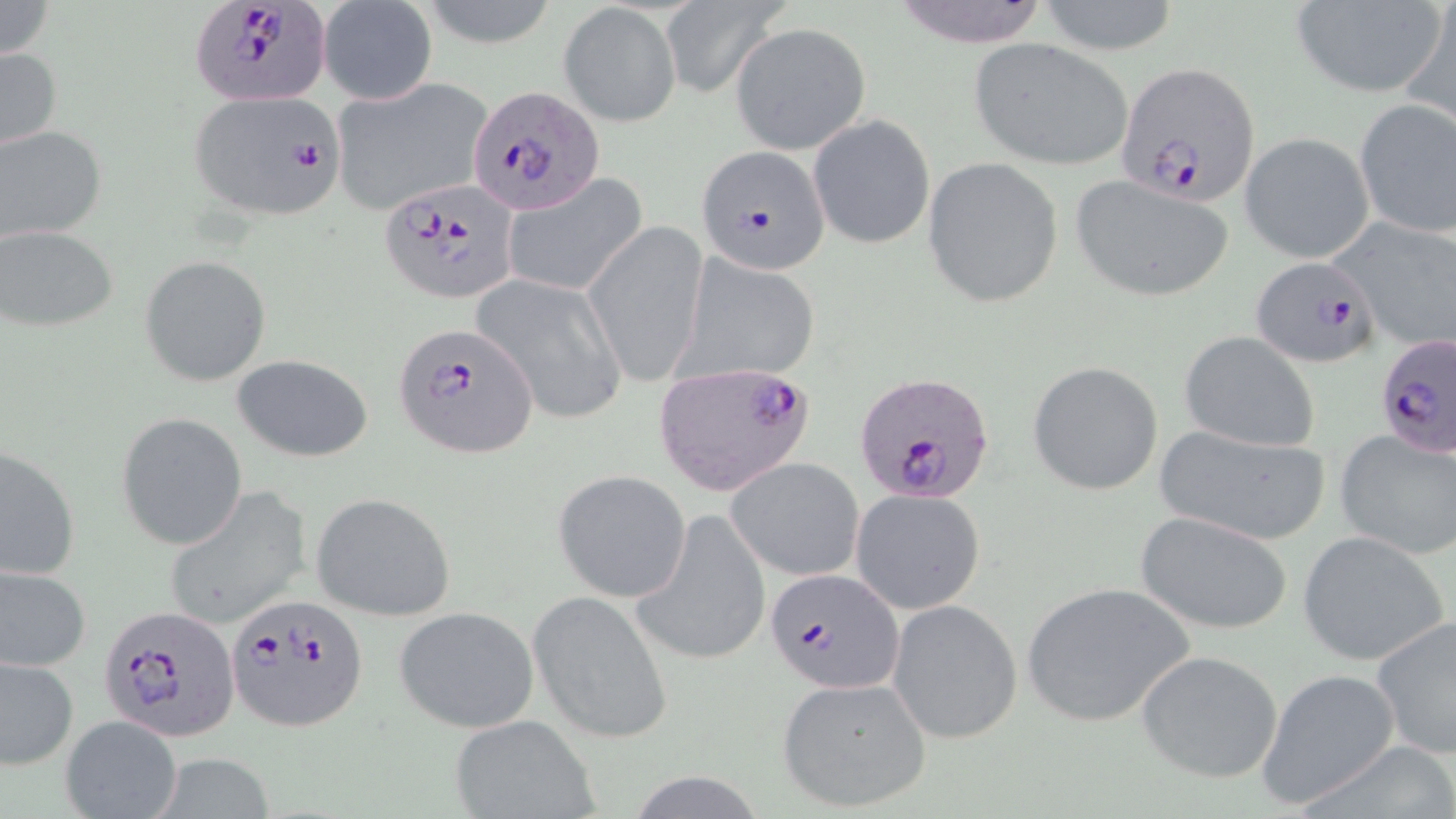

Approximate bounding boxes as (x1, y1, x2, y2) in pixels. Plasmodium falciparum-infected red blood cell locations: (190, 2, 332, 108), (1118, 63, 1258, 206), (467, 85, 605, 215), (192, 90, 344, 217), (695, 145, 830, 274), (377, 178, 518, 304), (1251, 257, 1382, 370), (391, 320, 537, 457), (1375, 333, 1456, 460), (654, 361, 816, 495), (857, 373, 996, 503), (765, 567, 904, 693), (226, 595, 367, 732), (96, 605, 238, 742). Uninfected red blood cell locations: (0, 0, 56, 60), (886, 0, 1056, 47), (1037, 0, 1183, 55), (658, 1, 785, 101), (1288, 1, 1448, 97), (1398, 1, 1456, 131), (318, 2, 438, 105), (560, 3, 679, 128), (731, 22, 871, 155), (969, 38, 1135, 170), (0, 42, 64, 155), (328, 76, 495, 217), (1355, 99, 1455, 240), (808, 113, 937, 251), (0, 123, 106, 243), (1239, 133, 1374, 264), (922, 158, 1063, 308), (499, 172, 651, 299), (1070, 174, 1235, 302), (1331, 218, 1456, 354), (584, 219, 710, 388), (0, 225, 119, 334), (680, 250, 821, 381), (138, 255, 271, 387), (473, 273, 627, 423), (1179, 332, 1319, 454), (230, 353, 374, 462), (1028, 361, 1163, 496), (118, 414, 247, 549), (1153, 422, 1331, 545), (1334, 427, 1456, 559), (0, 444, 80, 582), (728, 457, 864, 579), (554, 471, 691, 602), (164, 488, 313, 629), (851, 488, 986, 614), (311, 492, 457, 621), (634, 511, 771, 666), (1132, 512, 1293, 635), (1298, 531, 1449, 667), (1, 565, 91, 674), (1022, 581, 1197, 728), (528, 589, 673, 744), (887, 600, 1022, 743), (393, 605, 538, 732), (1372, 617, 1456, 759), (1135, 648, 1285, 784), (0, 654, 79, 770), (1258, 668, 1403, 806), (776, 677, 932, 813), (60, 714, 181, 819), (447, 714, 599, 819), (146, 756, 280, 818). Slide-level diagnosis: Plasmodium falciparum. Light microscopy. One field of a larger specimen. Image is 1456×819 pixels. Thin blood film. Captured at 1000x magnification. May-Grünwald-Giemsa stain.